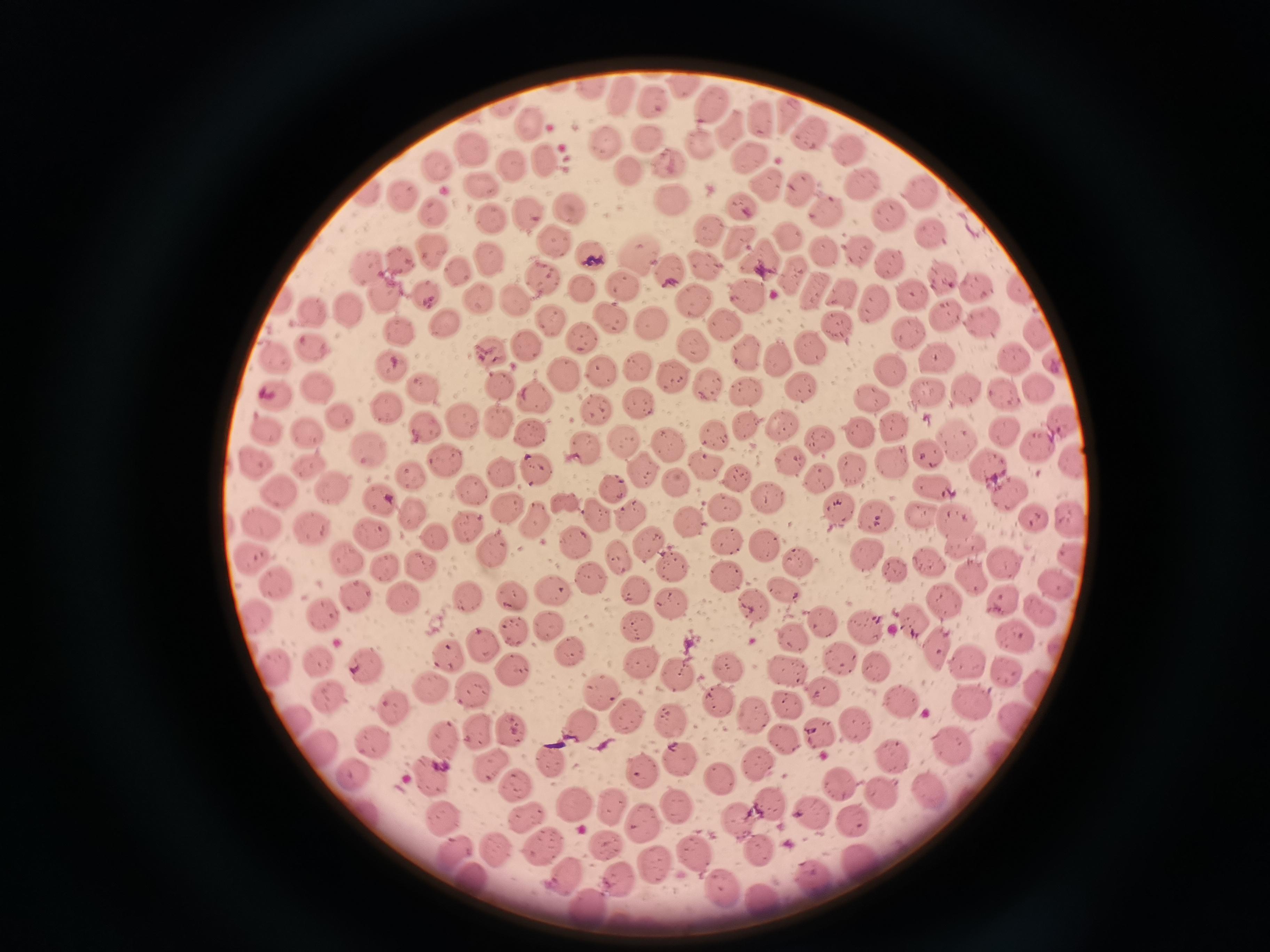
{
  "cell_locations": "approximate centers as {x, y} in pixels: {685, 82}, {589, 87}, {623, 91}, {653, 103}, {709, 105}, {785, 110}, {758, 120}, {528, 121}, {728, 125}, {804, 131}, {641, 140}, {606, 142}, {707, 142}, {471, 146}, {846, 147}, {545, 155}, {746, 158}, {674, 159}, {513, 165}, {434, 168}, {625, 172}, {856, 178}, {482, 181}, {767, 181}, {800, 185}, {920, 190}, {364, 193}, {405, 194}, {672, 196}, {740, 201}, {434, 209}, {826, 209}, {567, 210}, {526, 212}, {888, 215}, {491, 220}, {701, 228}, {927, 232}, {789, 234}, {733, 241}, {553, 242}, {433, 251}, {827, 251}, {853, 251}, {590, 254}, {397, 255}, {638, 257}, {889, 259}, {762, 260}, {491, 261}, {367, 263}, {669, 269}, {456, 271}, {791, 271}, {544, 275}, {944, 278}, {624, 283}, {385, 287}, {980, 287}, {584, 289}, {1024, 290}, {845, 292}, {424, 293}, {817, 293}, {514, 294}, {747, 295}, {911, 295}, {278, 296}, {475, 299}, {696, 301}, {871, 307}, {316, 309}, {346, 309}, {947, 316}, {611, 320}, {550, 321}, {650, 321}, {444, 322}, {723, 324}, {836, 327}, {984, 328}, {401, 330}, {911, 331}, {1039, 332}, {581, 336}, {694, 342}, {522, 345}, {313, 346}, {813, 346}, {493, 351}, {275, 353}, {742, 356}, {1014, 356}, {935, 358}, {637, 362}, {774, 363}, {387, 367}, {603, 371}, {887, 371}, {565, 373}, {673, 377}, {502, 381}, {704, 381}, {318, 383}, {796, 383}, {926, 386}, {1037, 386}, {425, 387}, {964, 388}, {742, 390}, {870, 392}, {275, 393}, {1000, 395}, {640, 399}, {534, 400}, {597, 406}, {387, 407}, {337, 414}, {782, 420}, {1060, 420}, {460, 421}, {499, 421}, {890, 421}, {268, 425}, {426, 425}, {746, 425}, {310, 428}, {853, 428}, {713, 429}, {1005, 431}, {532, 435}, {622, 436}, {955, 436}, {817, 439}, {666, 441}, {369, 446}, {584, 446}, {1037, 448}, {926, 456}, {255, 458}, {787, 459}, {890, 459}, {445, 460}, {703, 461}, {984, 462}, {305, 463}, {1074, 466}, {853, 467}, {539, 468}, {643, 468}, {507, 471}, {413, 473}, {733, 475}, {819, 475}, {675, 483}, {934, 483}, {613, 486}, {328, 487}, {273, 488}, {1006, 488}, {469, 489}, {381, 498}, {767, 498}, {722, 504}, {837, 505}, {503, 506}, {872, 511}, {410, 512}, {628, 512}, {920, 513}, {597, 515}, {1030, 517}, {688, 518}, {531, 519}, {953, 519}, {260, 520}, {1068, 522}, {312, 524}, {468, 524}, {372, 533}, {433, 539}, {729, 539}, {571, 540}, {648, 542}, {964, 542}, {766, 543}, {490, 547}, {616, 555}, {347, 557}, {865, 557}, {801, 558}, {250, 559}, {1000, 561}, {929, 562}, {1073, 562}, {675, 564}, {386, 565}, {426, 565}, {895, 571}, {724, 574}, {590, 577}, {277, 585}, {1055, 585}, {785, 586}, {553, 587}, {632, 588}, {356, 592}, {510, 594}, {1004, 596}, {942, 597}, {463, 598}, {402, 599}, {671, 606}, {754, 606}, {1039, 607}, {325, 610}, {257, 615}, {637, 621}, {826, 621}, {908, 623}, {548, 625}, {863, 625}, {514, 631}, {1011, 634}, {795, 637}, {485, 645}, {568, 650}, {938, 651}, {445, 652}, {844, 653}, {319, 655}, {967, 658}, {638, 660}, {879, 664}, {363, 666}, {730, 666}, {274, 667}, {514, 668}, {1008, 671}, {786, 672}, {679, 675}, {472, 686}, {430, 689}, {816, 689}, {328, 692}, {897, 693}, {598, 694}, {719, 699}, {389, 702}, {788, 703}, {974, 703}, {623, 714}, {756, 716}, {672, 718}, {1014, 718}, {296, 719}, {851, 722}, {512, 727}, {479, 728}, {580, 729}, {820, 736}, {444, 740}, {377, 742}, {784, 743}, {953, 744}, {316, 747}, {891, 752}, {550, 756}, {682, 758}, {761, 760}, {492, 763}, {640, 770}, {352, 774}, {433, 775}, {716, 779}, {515, 782}, {843, 783}, {879, 787}, {929, 788}, {573, 800}, {768, 802}, {607, 805}, {673, 805}, {810, 811}, {362, 813}, {445, 813}, {528, 816}, {852, 816}, {736, 819}, {644, 821}, {538, 844}, {603, 845}, {493, 849}, {449, 850}, {688, 851}, {759, 851}, {860, 860}, {653, 868}, {561, 874}, {467, 877}, {621, 879}, {813, 879}, {719, 886}, {761, 902}, {589, 907}",
  "capture": "smartphone through the microscope eyepiece",
  "stain": "Giemsa",
  "image_size": "1270×952 pixels",
  "field_of_view": "single",
  "preparation": "thin blood smear"
}